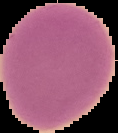

Summary:
  - Preparation: thin blood film
  - Image size: 118×133 pixels
  - Image type: cell region segmented out of the field of view; surrounding area masked to black
  - Malaria status: uninfected